Assess the morphology of the red blood cells.
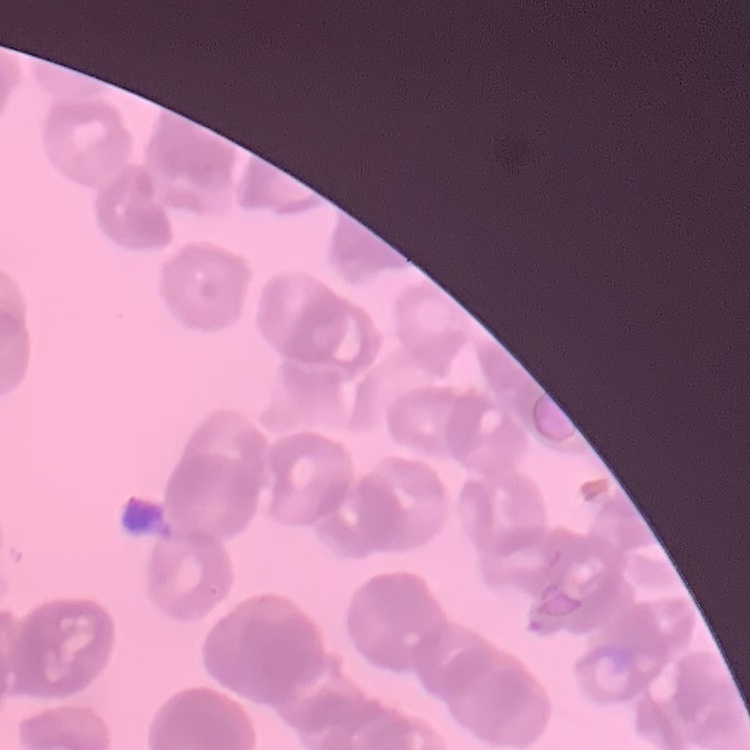

They show rouleaux formation.

Summary:
  - Preparation: thin blood film
  - Stain: Field's or Giemsa
  - Image type: square crop of a larger photomicrograph